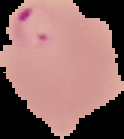 From a thin blood film. Result: Plasmodium parasites detected. Image is 124×139 pixels. Cell region segmented out of the field of view; the surrounding area is masked to black.